Locate every blood parasite and identify its species.
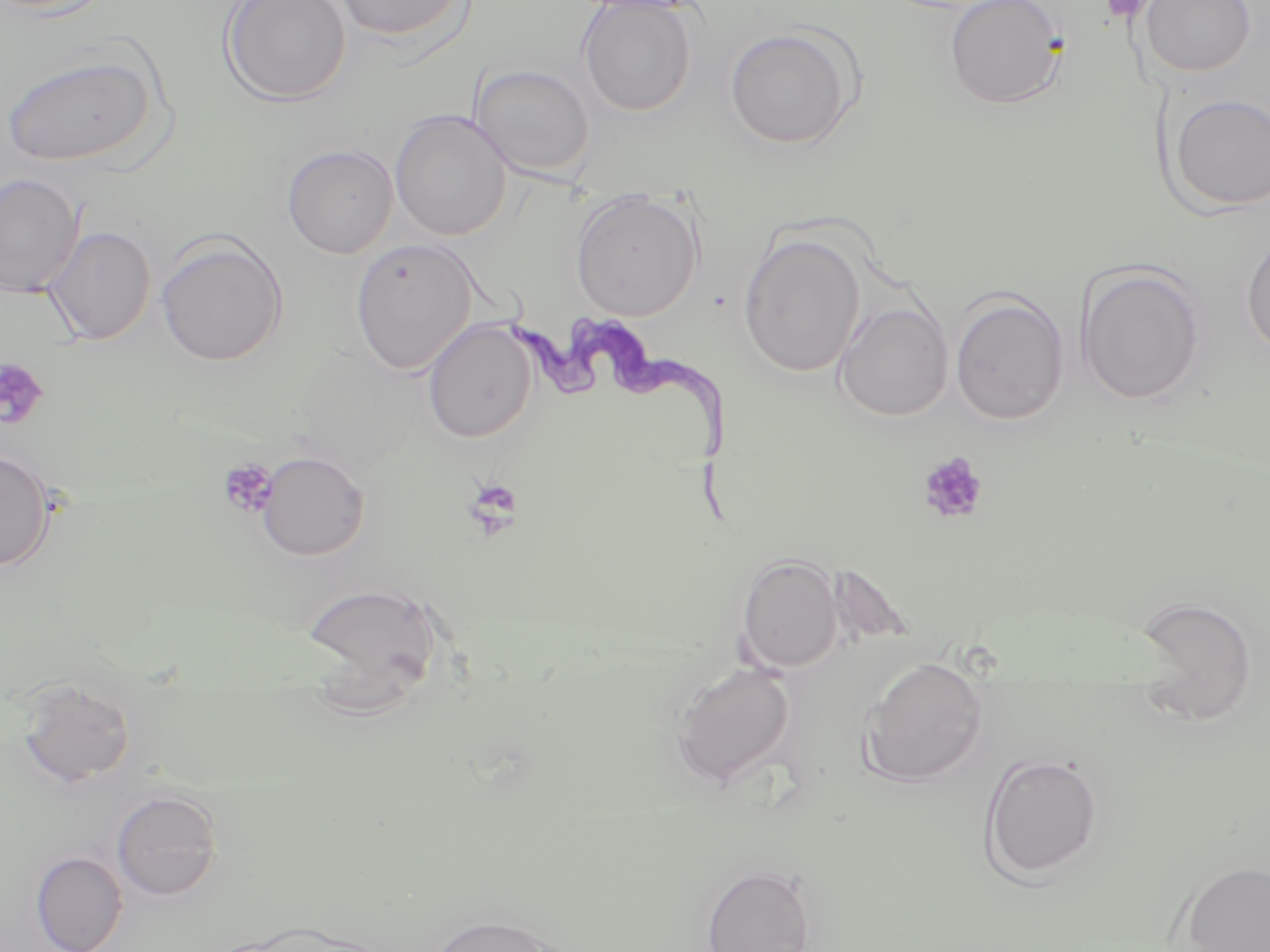
Approximate bounding boxes as named x1/y1/x2/y2 corners in pixels.
Trypanosoma brucei: (x1=506, y1=313, x2=742, y2=521).
No Plasmodium falciparum, Plasmodium ovale, Plasmodium malariae, Plasmodium vivax, or Babesia divergens observed.

Platelet locations: (x1=1100, y1=0, x2=1155, y2=24), (x1=0, y1=357, x2=49, y2=430), (x1=917, y1=450, x2=989, y2=526), (x1=217, y1=459, x2=279, y2=519), (x1=462, y1=478, x2=524, y2=538). Uninfected red blood cell locations: (x1=220, y1=0, x2=351, y2=107), (x1=330, y1=0, x2=470, y2=41), (x1=943, y1=0, x2=1067, y2=110), (x1=1140, y1=0, x2=1255, y2=77), (x1=578, y1=1, x2=697, y2=116), (x1=724, y1=27, x2=858, y2=150), (x1=2, y1=53, x2=157, y2=167), (x1=469, y1=63, x2=595, y2=179), (x1=1165, y1=93, x2=1270, y2=213), (x1=389, y1=109, x2=512, y2=241), (x1=281, y1=143, x2=399, y2=259), (x1=0, y1=173, x2=84, y2=298), (x1=570, y1=189, x2=704, y2=322), (x1=42, y1=225, x2=156, y2=346), (x1=1241, y1=228, x2=1270, y2=362), (x1=37, y1=229, x2=281, y2=349), (x1=155, y1=233, x2=288, y2=368), (x1=738, y1=233, x2=866, y2=378), (x1=349, y1=238, x2=479, y2=375), (x1=1075, y1=263, x2=1205, y2=406), (x1=949, y1=291, x2=1070, y2=426), (x1=833, y1=301, x2=953, y2=421), (x1=422, y1=319, x2=537, y2=444), (x1=0, y1=449, x2=56, y2=572), (x1=256, y1=451, x2=370, y2=561), (x1=736, y1=552, x2=844, y2=674), (x1=299, y1=580, x2=445, y2=699), (x1=1129, y1=594, x2=1259, y2=727), (x1=860, y1=655, x2=990, y2=788), (x1=670, y1=662, x2=797, y2=789), (x1=14, y1=676, x2=136, y2=788), (x1=978, y1=752, x2=1104, y2=884), (x1=111, y1=789, x2=223, y2=901), (x1=29, y1=850, x2=128, y2=952), (x1=1179, y1=861, x2=1270, y2=952), (x1=700, y1=863, x2=817, y2=952), (x1=426, y1=910, x2=569, y2=952). Slide-level diagnosis: Trypanosoma brucei. Optical microscopy. Image is 1270×952 pixels. Single field of view. 1000x magnification. Thin blood film. May-Grünwald-Giemsa stain.